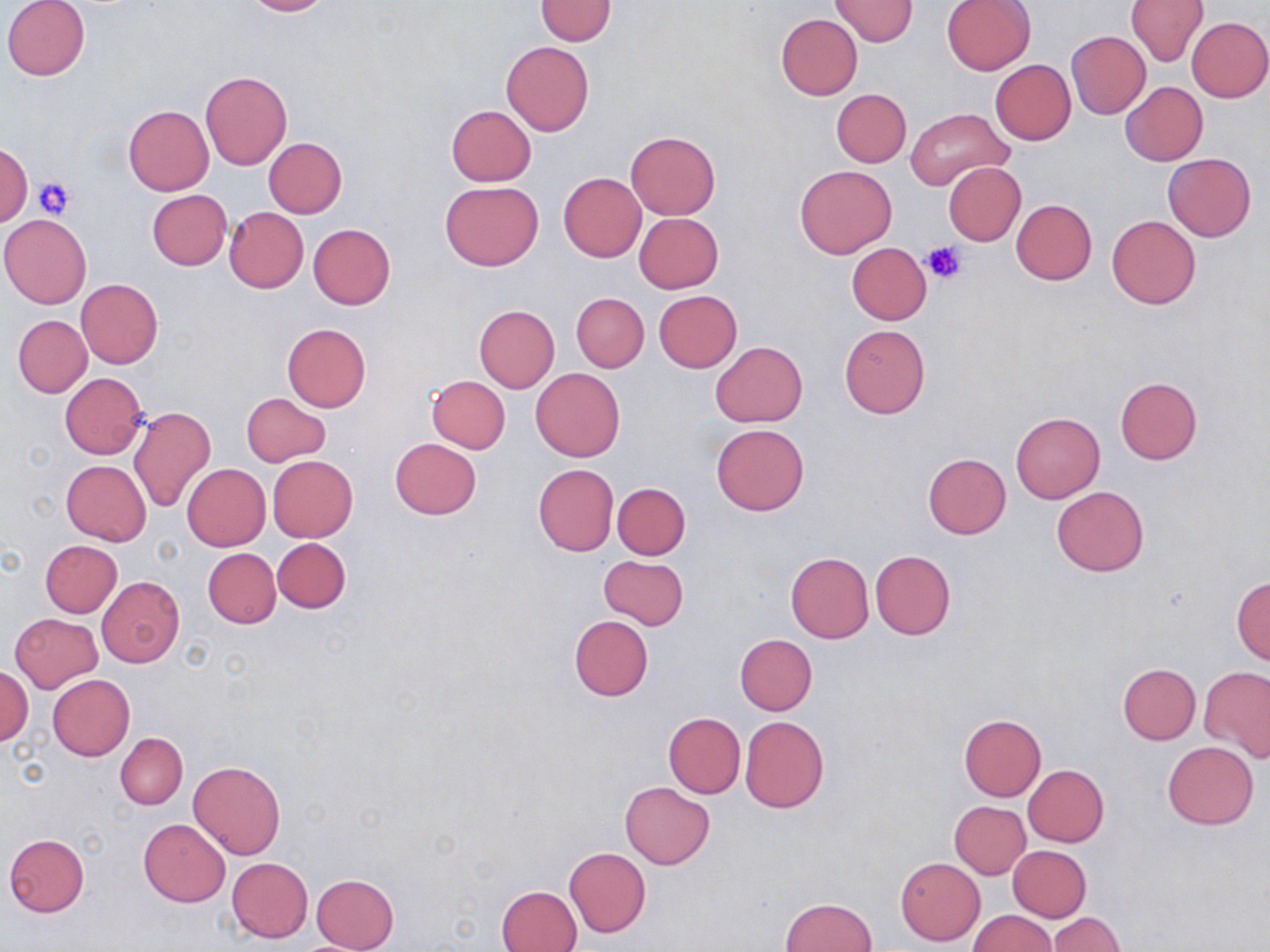

{
  "slide_level_diagnosis": "no evidence of blood parasites",
  "stain": "May-Grünwald-Giemsa",
  "platelet_locations": "approximate bounding boxes as named x1/y1/x2/y2 corners in pixels: (x1=35, y1=176, x2=78, y2=220), (x1=923, y1=240, x2=969, y2=284)",
  "magnification": "1000x",
  "field_of_view": "single",
  "image_size": "1270×952 pixels",
  "preparation": "thin blood smear",
  "modality": "optical microscopy",
  "uninfected_red_blood_cell_locations": "approximate bounding boxes as named x1/y1/x2/y2 corners in pixels: (x1=2, y1=0, x2=90, y2=82), (x1=242, y1=0, x2=332, y2=17), (x1=534, y1=0, x2=617, y2=45), (x1=830, y1=0, x2=917, y2=46), (x1=942, y1=0, x2=1035, y2=74), (x1=1124, y1=0, x2=1208, y2=67), (x1=1127, y1=7, x2=1268, y2=86), (x1=775, y1=14, x2=863, y2=100), (x1=1187, y1=16, x2=1269, y2=102), (x1=1066, y1=31, x2=1151, y2=118), (x1=501, y1=41, x2=593, y2=136), (x1=989, y1=59, x2=1076, y2=145), (x1=200, y1=71, x2=291, y2=170), (x1=1121, y1=82, x2=1207, y2=166), (x1=832, y1=89, x2=911, y2=166), (x1=124, y1=105, x2=213, y2=195), (x1=447, y1=105, x2=536, y2=185), (x1=906, y1=108, x2=1012, y2=189), (x1=625, y1=131, x2=719, y2=220), (x1=264, y1=138, x2=347, y2=218), (x1=0, y1=142, x2=32, y2=226), (x1=1164, y1=153, x2=1256, y2=241), (x1=943, y1=162, x2=1026, y2=245), (x1=795, y1=164, x2=897, y2=259), (x1=558, y1=173, x2=646, y2=262), (x1=441, y1=181, x2=543, y2=270), (x1=146, y1=189, x2=232, y2=271), (x1=1011, y1=199, x2=1097, y2=285), (x1=224, y1=207, x2=308, y2=292), (x1=634, y1=213, x2=723, y2=293), (x1=1106, y1=213, x2=1201, y2=309), (x1=0, y1=214, x2=91, y2=309), (x1=308, y1=223, x2=396, y2=309), (x1=846, y1=242, x2=933, y2=325), (x1=76, y1=278, x2=163, y2=368), (x1=654, y1=291, x2=742, y2=372), (x1=571, y1=292, x2=649, y2=373), (x1=474, y1=305, x2=559, y2=393), (x1=12, y1=315, x2=92, y2=397), (x1=281, y1=323, x2=371, y2=412), (x1=839, y1=324, x2=931, y2=418), (x1=710, y1=341, x2=807, y2=427), (x1=530, y1=368, x2=625, y2=462), (x1=59, y1=374, x2=147, y2=459), (x1=426, y1=375, x2=510, y2=453), (x1=1115, y1=377, x2=1202, y2=465), (x1=242, y1=392, x2=331, y2=467), (x1=128, y1=406, x2=216, y2=512), (x1=1011, y1=412, x2=1105, y2=503), (x1=710, y1=424, x2=809, y2=516), (x1=390, y1=439, x2=481, y2=518), (x1=922, y1=453, x2=1012, y2=540), (x1=267, y1=455, x2=358, y2=541), (x1=61, y1=460, x2=150, y2=545), (x1=182, y1=463, x2=271, y2=550), (x1=533, y1=463, x2=618, y2=556), (x1=612, y1=482, x2=690, y2=559), (x1=1051, y1=487, x2=1148, y2=576), (x1=273, y1=537, x2=351, y2=612), (x1=40, y1=540, x2=122, y2=617), (x1=203, y1=548, x2=280, y2=628), (x1=870, y1=549, x2=956, y2=639), (x1=785, y1=553, x2=874, y2=643), (x1=599, y1=555, x2=689, y2=630), (x1=582, y1=560, x2=680, y2=694), (x1=98, y1=576, x2=184, y2=667), (x1=1231, y1=576, x2=1270, y2=666), (x1=10, y1=613, x2=103, y2=692), (x1=569, y1=615, x2=653, y2=700), (x1=734, y1=634, x2=817, y2=716), (x1=1117, y1=663, x2=1201, y2=744), (x1=1, y1=665, x2=32, y2=745), (x1=1200, y1=666, x2=1270, y2=762), (x1=48, y1=674, x2=134, y2=760), (x1=662, y1=712, x2=745, y2=798), (x1=958, y1=714, x2=1047, y2=801), (x1=740, y1=716, x2=829, y2=814), (x1=116, y1=732, x2=187, y2=809), (x1=1162, y1=741, x2=1258, y2=829), (x1=189, y1=760, x2=286, y2=860), (x1=1024, y1=765, x2=1109, y2=847), (x1=621, y1=782, x2=713, y2=868), (x1=949, y1=801, x2=1030, y2=879), (x1=138, y1=819, x2=230, y2=906), (x1=4, y1=834, x2=89, y2=916), (x1=1007, y1=845, x2=1092, y2=922), (x1=564, y1=847, x2=650, y2=938), (x1=226, y1=857, x2=314, y2=943), (x1=895, y1=858, x2=984, y2=945), (x1=311, y1=873, x2=399, y2=952), (x1=496, y1=884, x2=583, y2=952), (x1=781, y1=897, x2=877, y2=951), (x1=969, y1=910, x2=1056, y2=952), (x1=1047, y1=913, x2=1123, y2=951)"
}